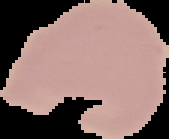

Segmented cell region on a black background. Result: no Plasmodium parasites detected. From a thin blood film. Image is 169×139 pixels.